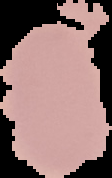

preparation = thin blood smear
malaria status = uninfected
image size = 112×178 pixels
image type = cell region segmented out of the field of view; surrounding area masked to black